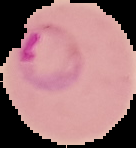
Summary:
  - Preparation: thin blood smear
  - Image type: segmented cell region on a black background
  - Malaria status: parasitized
  - Image size: 136×148 pixels